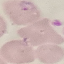

result: malaria parasites detected
stain: Giemsa
capture: smartphone through the microscope eyepiece
preparation: thin smear
image_type: cell patch, automatically extracted from a larger field of view and resized to 64 × 64 pixels